Classify this cell by malaria status.
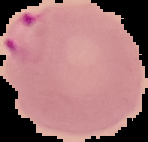
Parasitized.

Summary:
  - Preparation: thin blood smear
  - Image type: segmented cell region with the area outside set to black
  - Image size: 148×142 pixels